Comment on the morphology of the red blood cells.
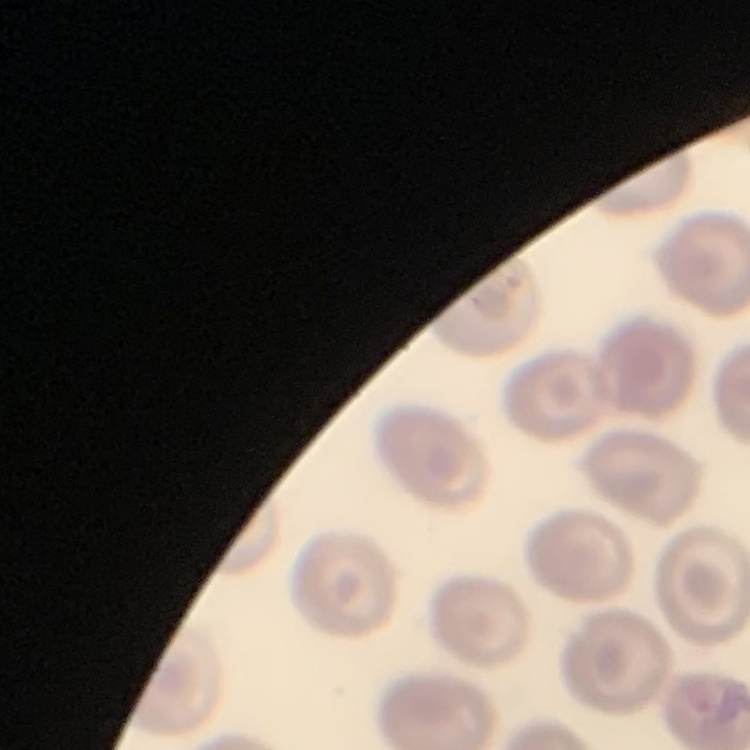

They show no rouleaux formation.

Thin blood smear. Square crop of a larger photomicrograph. Stained with either Field's or Giemsa.